Locate the cells, classifying each as a parasitized RBC, an uninfected RBC, or a WBC.
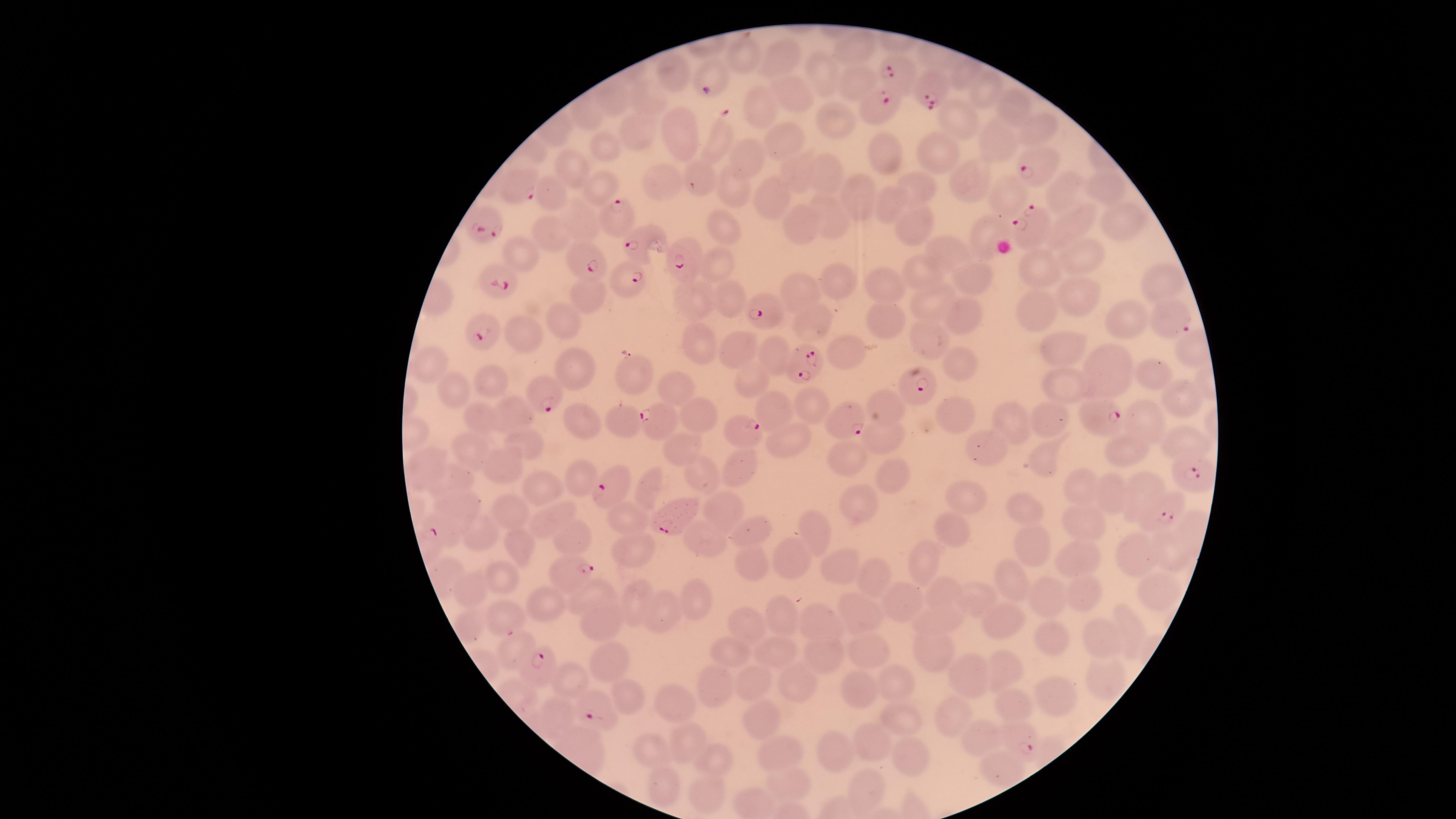

Approximate marker points as {x, y} in pixels.
Parasitized RBCs: {900, 73}, {712, 77}, {932, 85}, {878, 106}, {1040, 162}, {522, 183}, {610, 213}, {489, 221}, {1031, 228}, {638, 241}, {583, 256}, {687, 257}, {630, 271}, {495, 276}, {766, 310}, {1172, 319}, {482, 334}, {802, 363}, {911, 389}, {546, 390}, {1096, 415}, {849, 416}, {658, 424}, {742, 426}, {1187, 470}, {611, 488}, {1163, 512}, {675, 514}, {442, 529}, {566, 569}, {541, 667}, {599, 709}, {1016, 737}.
Uninfected RBCs: {860, 50}, {741, 55}, {782, 57}, {822, 69}, {678, 71}, {852, 78}, {986, 87}, {786, 92}, {650, 105}, {1017, 105}, {762, 110}, {955, 110}, {832, 120}, {1037, 125}, {640, 130}, {681, 132}, {784, 134}, {995, 144}, {604, 145}, {883, 146}, {943, 151}, {751, 154}, {795, 167}, {574, 168}, {825, 170}, {961, 176}, {917, 182}, {661, 183}, {1097, 184}, {600, 186}, {1058, 187}, {733, 188}, {865, 189}, {770, 195}, {1000, 195}, {549, 196}, {889, 201}, {834, 217}, {1121, 218}, {579, 220}, {806, 220}, {1076, 222}, {720, 225}, {917, 226}, {988, 231}, {550, 233}, {949, 249}, {516, 250}, {1080, 256}, {1034, 263}, {719, 264}, {920, 271}, {970, 277}, {884, 279}, {840, 280}, {1166, 281}, {801, 290}, {590, 292}, {725, 296}, {1085, 296}, {696, 298}, {1038, 306}, {935, 308}, {1136, 314}, {972, 315}, {820, 316}, {884, 316}, {568, 317}, {526, 337}, {926, 339}, {702, 340}, {1184, 344}, {1066, 346}, {743, 347}, {846, 352}, {771, 353}, {432, 363}, {574, 366}, {957, 368}, {1108, 368}, {750, 371}, {1154, 373}, {631, 374}, {495, 378}, {1065, 387}, {455, 388}, {676, 391}, {1181, 394}, {809, 404}, {699, 406}, {778, 407}, {886, 408}, {517, 413}, {486, 416}, {960, 416}, {1015, 418}, {1045, 418}, {580, 419}, {622, 420}, {1144, 422}, {887, 436}, {789, 437}, {1182, 439}, {531, 442}, {985, 445}, {1128, 447}, {475, 451}, {847, 452}, {1042, 453}, {502, 463}, {742, 467}, {581, 472}, {887, 472}, {456, 477}, {544, 487}, {1077, 487}, {1140, 487}, {650, 490}, {971, 493}, {1109, 493}, {452, 502}, {863, 505}, {1024, 506}, {722, 507}, {514, 512}, {554, 513}, {631, 514}, {1074, 520}, {816, 529}, {951, 529}, {480, 530}, {756, 530}, {574, 539}, {701, 539}, {517, 541}, {1034, 545}, {637, 548}, {1128, 550}, {1175, 550}, {929, 557}, {1078, 557}, {839, 558}, {793, 559}, {756, 562}, {865, 571}, {500, 574}, {1013, 582}, {945, 588}, {601, 589}, {1160, 589}, {472, 590}, {1079, 592}, {1047, 594}, {697, 596}, {635, 597}, {978, 597}, {907, 601}, {542, 605}, {666, 607}, {860, 611}, {785, 612}, {1005, 614}, {601, 615}, {505, 618}, {821, 618}, {1129, 620}, {755, 621}, {947, 623}, {1046, 631}, {1101, 634}, {516, 645}, {732, 646}, {865, 647}, {781, 648}, {934, 651}, {818, 653}, {607, 657}, {1006, 668}, {973, 674}, {799, 679}, {1107, 679}, {757, 681}, {721, 682}, {897, 682}, {575, 683}, {866, 689}, {626, 691}, {673, 699}, {1061, 700}, {1015, 702}, {553, 709}, {753, 713}, {950, 715}, {905, 723}, {688, 734}, {977, 736}, {871, 747}, {651, 749}, {836, 750}, {777, 752}, {713, 761}, {911, 762}, {1002, 770}, {786, 786}, {868, 787}, {661, 790}, {710, 791}.
No WBCs identified.

Image is 1456×819 pixels. Thin blood film. Circular visible region. Single field of view. Giemsa stain. Smartphone photograph through the microscope eyepiece. Species: Plasmodium falciparum.